Point out each malaria parasite.
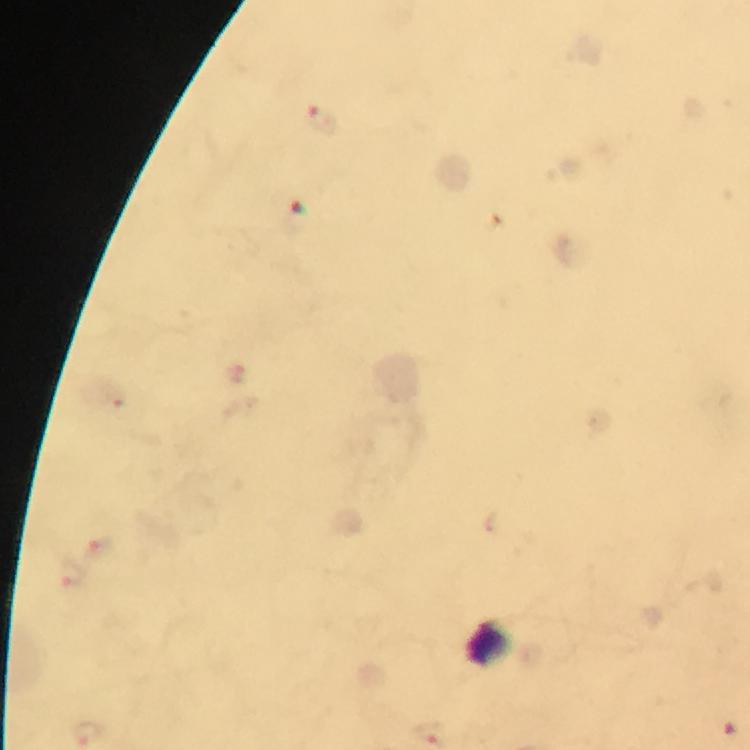

Approximate centers as (x, y) in pixels.
Malaria parasites: (325, 120).

preparation = thick blood smear
capture = smartphone camera through the microscope
stain = Giemsa
magnification = 100x
cropped from = one field of view
context = from a diagnostic examination for malaria
image size = 750×750 pixels
immersion oil = used